Report the malaria status of this cell.
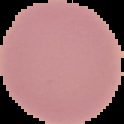

Uninfected.

preparation = thin blood film
image type = cell region segmented out of the field of view; surrounding area masked to black
image size = 124×124 pixels